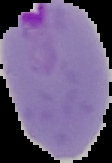
preparation = thin blood film
result = Plasmodium parasites detected
image size = 112×163 pixels
image type = segmented cell region on a black background